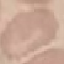

Summary:
  - Malaria status: uninfected
  - Preparation: thin blood film
  - Stain: Giemsa
  - Image type: automatically extracted cell patch, resized to 64 × 64 pixels
  - Capture: smartphone through the microscope eyepiece